Point out each Plasmodium parasite.
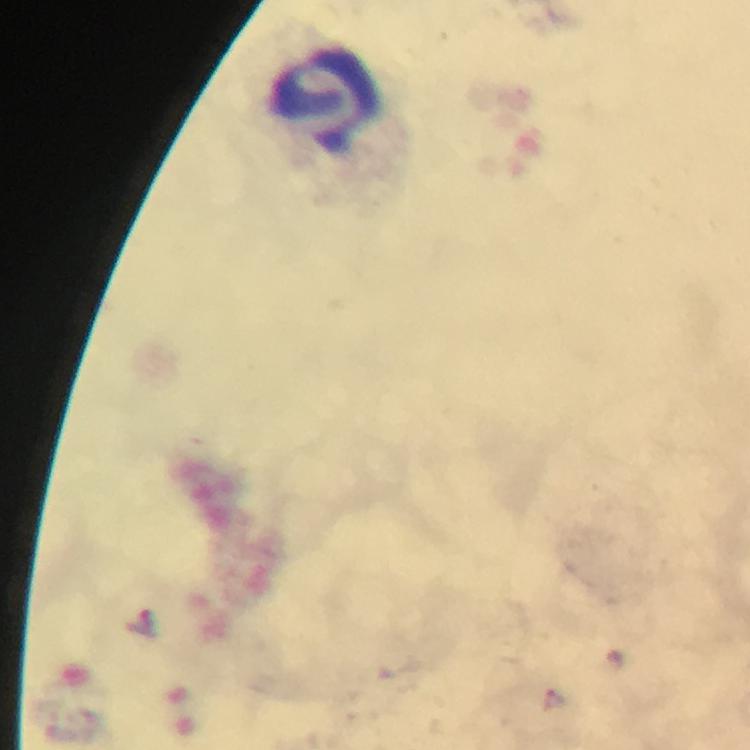

No Plasmodium parasites detected.

Approximate object centers, in pixels from the top-left corner.
Summary:
  - Leukocyte locations: (x=322, y=101)
  - Magnification: 100x
  - Preparation: thick blood film
  - Cropped from: one field of view
  - Context: from a malaria diagnostic workup
  - Stain: Giemsa
  - Immersion oil: used
  - Image size: 750×750 pixels
  - Capture: smartphone camera through the microscope